State which parasite is depicted.
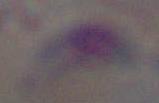
This is Toxoplasma gondii.

Captured at 1000x magnification. Photomicrograph.